Evaluate for Plasmodium parasites.
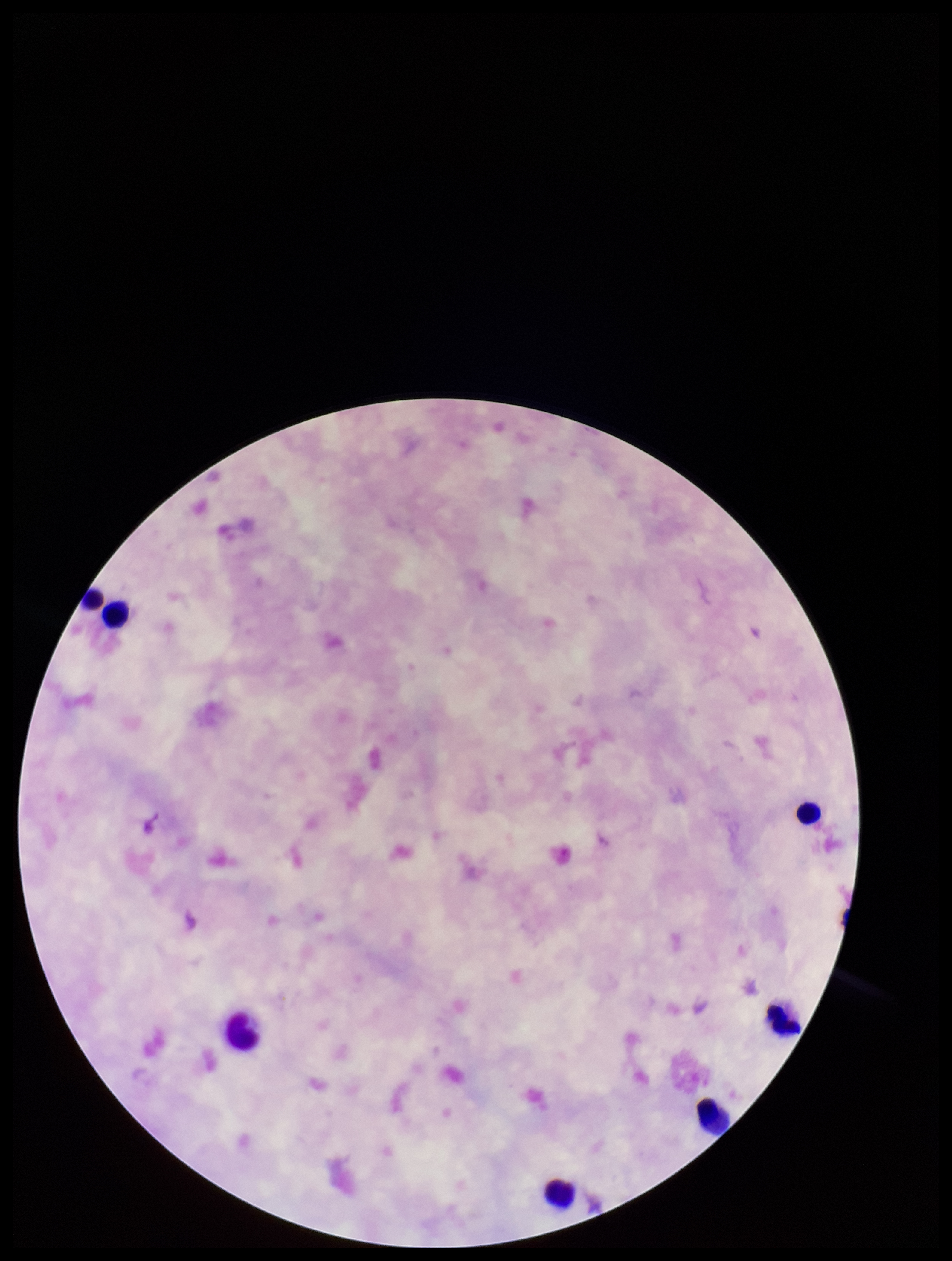

None detected.

Leukocyte count: 7. Giemsa stain. Image is 952×1261 pixels. Patient malaria status: negative. Parasite count: 0. Preparation: thick smear. Photographed through the microscope eyepiece with a smartphone camera. Single field of view.